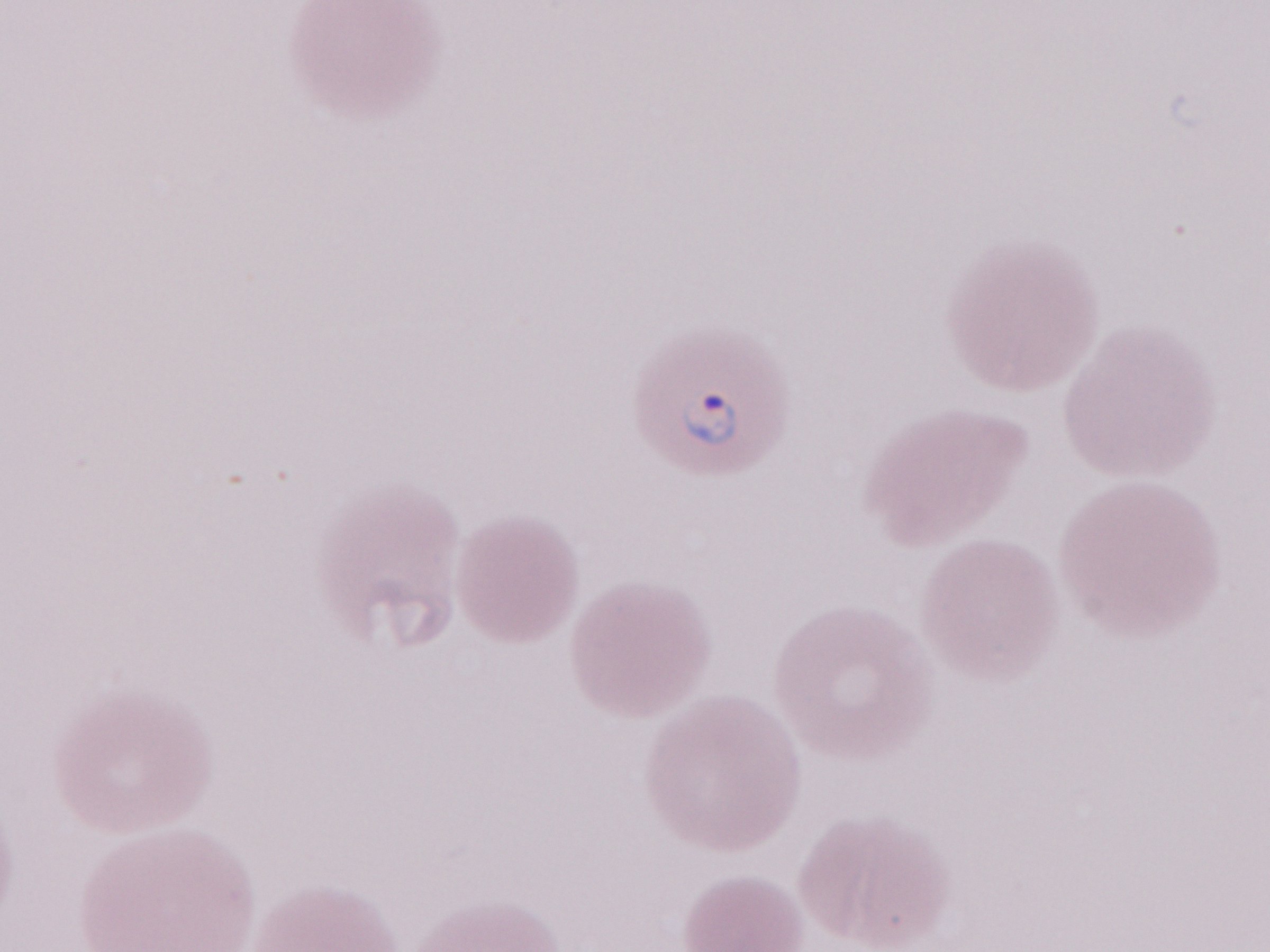
One field of this slide. Malaria diagnosis (patient-level): positive. Image is 1270×952 pixels. Thin blood film. May-Grünwald-Giemsa stain. Magnification: 1,000x. Olympus BX43 microscope, Olympus DP73 camera.